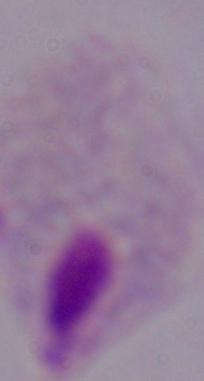
Summary:
  - Magnification: 1000x
  - Identification: trichomonad
  - Modality: micrograph